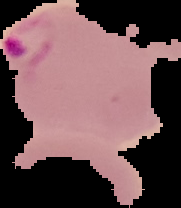

Cell region segmented out of the field of view; the surrounding area is masked to black. Image is 181×208 pixels. From a thin blood smear. Result: malaria parasites detected.